Report the malaria status of this cell.
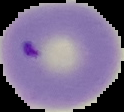
Parasitized.

Summary:
  - Image type: segmented cell region with the area outside set to black
  - Image size: 124×112 pixels
  - Preparation: thin blood smear